Assess the morphology of the erythrocytes.
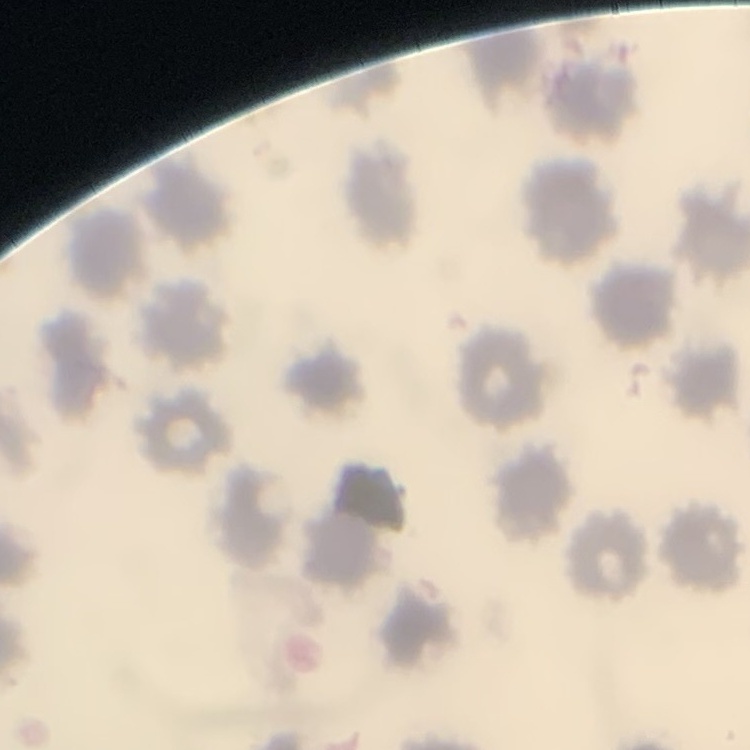
They show no rouleaux formation.

One tile cut from a larger photomicrograph. Stained with either Field's or Giemsa. Thin blood film.